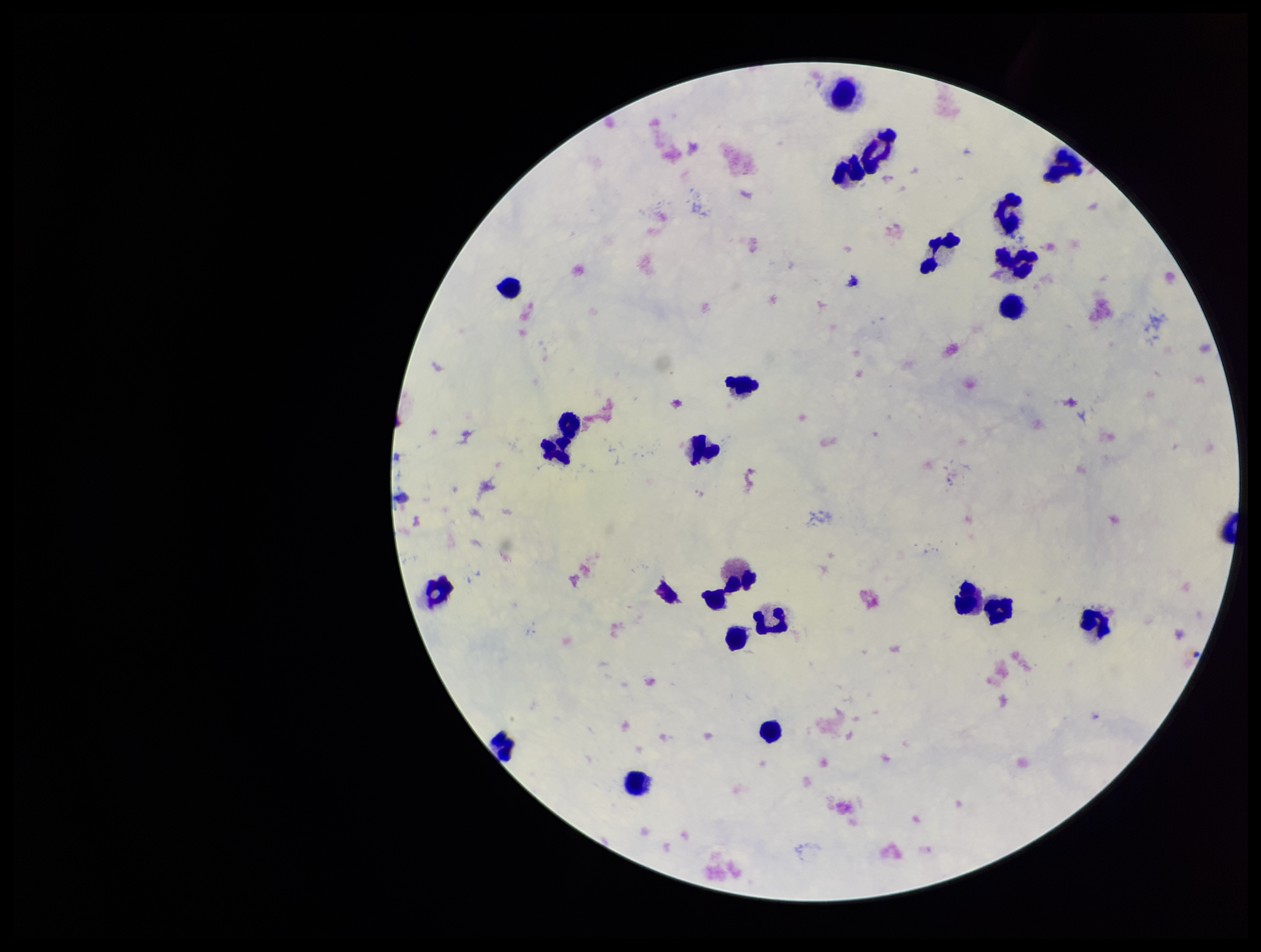
Summary:
  - Capture: smartphone photograph through the microscope eyepiece
  - Stain: Giemsa
  - Image size: 1261×952 pixels
  - Plasmodium parasites: none seen
  - Patient malaria status: negative
  - Field of view: single
  - Preparation: thick smear
  - Leukocyte count: 23
  - Parasite count: 0